Outline each blood parasite and name the species.
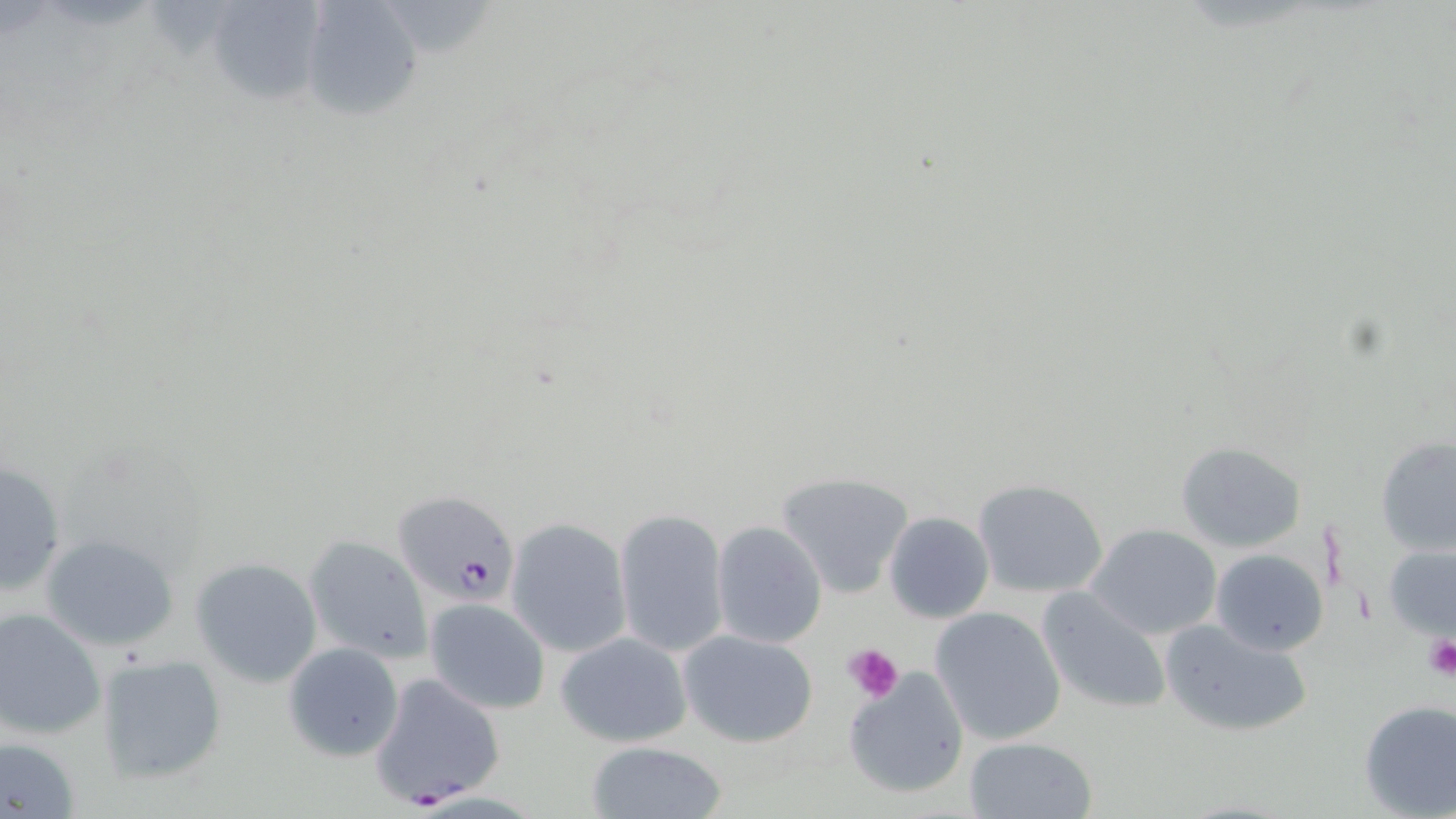

Approximate bounding boxes as named x1/y1/x2/y2 corners in pixels.
Plasmodium falciparum-infected red blood cells: (x1=392, y1=490, x2=522, y2=607), (x1=369, y1=672, x2=506, y2=806).
No Plasmodium ovale, Plasmodium malariae, Plasmodium vivax, Babesia divergens, or Trypanosoma brucei observed.

Uninfected red blood cell locations: (x1=204, y1=2, x2=328, y2=102), (x1=299, y1=2, x2=420, y2=120), (x1=1376, y1=434, x2=1456, y2=558), (x1=1174, y1=441, x2=1309, y2=555), (x1=0, y1=456, x2=67, y2=596), (x1=776, y1=469, x2=916, y2=597), (x1=972, y1=478, x2=1107, y2=599), (x1=613, y1=507, x2=729, y2=659), (x1=882, y1=510, x2=994, y2=622), (x1=505, y1=517, x2=633, y2=659), (x1=709, y1=519, x2=828, y2=648), (x1=1086, y1=523, x2=1221, y2=640), (x1=38, y1=532, x2=180, y2=651), (x1=302, y1=533, x2=435, y2=665), (x1=1383, y1=544, x2=1454, y2=640), (x1=1209, y1=548, x2=1328, y2=656), (x1=189, y1=557, x2=325, y2=687), (x1=1036, y1=587, x2=1172, y2=713), (x1=424, y1=597, x2=550, y2=715), (x1=928, y1=605, x2=1067, y2=746), (x1=0, y1=609, x2=106, y2=740), (x1=1158, y1=615, x2=1315, y2=739), (x1=680, y1=630, x2=819, y2=748), (x1=555, y1=631, x2=694, y2=747), (x1=282, y1=641, x2=404, y2=761), (x1=94, y1=652, x2=227, y2=787), (x1=842, y1=665, x2=969, y2=798), (x1=1356, y1=699, x2=1456, y2=819), (x1=0, y1=735, x2=80, y2=816), (x1=962, y1=735, x2=1097, y2=819), (x1=584, y1=741, x2=730, y2=819). Platelet locations: (x1=1425, y1=639, x2=1456, y2=680), (x1=844, y1=642, x2=904, y2=702). Slide-level diagnosis: Plasmodium falciparum. Captured at 1000x magnification. One field of a larger specimen. Image is 1456×819 pixels. Thin blood film. Light microscopy. May-Grünwald-Giemsa stain.